Assess this cell for malaria.
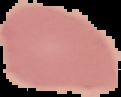

It is uninfected.

Summary:
  - Preparation: thin blood film
  - Image size: 121×97 pixels
  - Image type: cell region segmented out of the field of view; surrounding area masked to black